State which cell type is depicted.
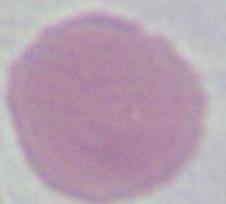

An erythrocyte.

Summary:
  - Modality: photomicrograph
  - Magnification: 1000x